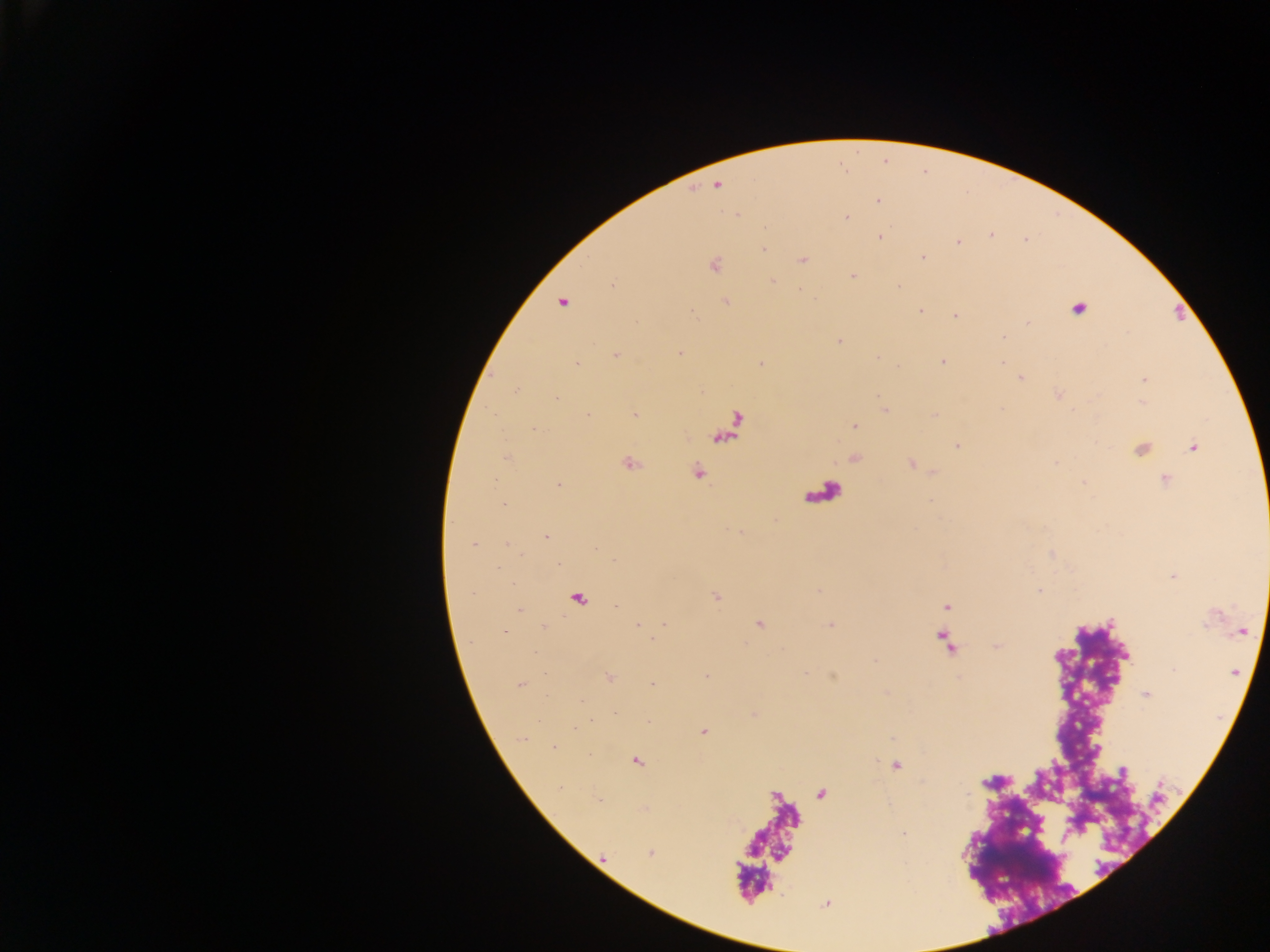
malaria parasite locations = approximate centers as [x, y] in pixels: [717, 184], [877, 200], [736, 215], [845, 217], [879, 236], [958, 243], [764, 248], [922, 258], [802, 259], [713, 264], [853, 275], [772, 281], [898, 287], [726, 301], [562, 302], [1077, 308], [920, 310], [956, 315], [1003, 336], [839, 341], [679, 352], [615, 354], [877, 357], [942, 360], [576, 363], [761, 363], [1019, 377], [1144, 378], [1059, 394], [885, 410], [635, 415], [933, 416], [854, 425], [535, 428], [957, 445], [1192, 447], [1140, 449], [506, 456], [854, 457], [629, 463], [912, 463], [696, 471], [934, 471], [1165, 479], [1083, 482], [558, 484], [502, 503], [546, 536], [472, 544], [1174, 575], [1039, 590], [716, 596], [577, 598], [947, 606], [758, 623], [638, 625], [830, 625], [543, 626], [504, 630], [1241, 631], [876, 661], [1234, 671], [608, 676], [706, 676], [652, 684], [520, 685], [1145, 693], [581, 699], [703, 731], [554, 747], [636, 760], [895, 765], [651, 852], [826, 902]
preparation = thick blood smear
field of view = single
capture = mobile-phone photograph through a microscope
country = Ghana
leukocyte locations = approximate centers as [x, y] in pixels: [822, 493]
image size = 1270×952 pixels